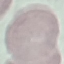
Result: negative for malaria parasites. Cell patch, automatically extracted from a larger field of view and resized to 64 × 64 pixels. Giemsa stain. Thin smear of blood. Acquired by smartphone through the microscope eyepiece.